Assess this cell for malaria.
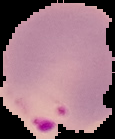
Parasitized.

Summary:
  - Image type: segmented cell region with the area outside set to black
  - Image size: 115×139 pixels
  - Preparation: thin blood film